Assess the morphology of the red blood cells.
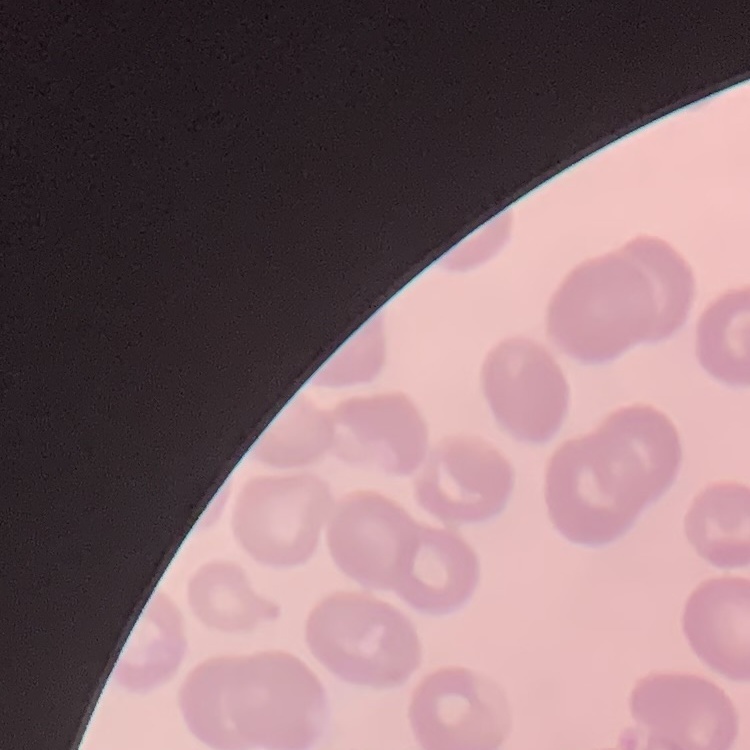
No rouleaux formation.

image type = one tile cut from a larger photomicrograph
preparation = thin blood film
stain = Field's or Giemsa